Locate platelets.
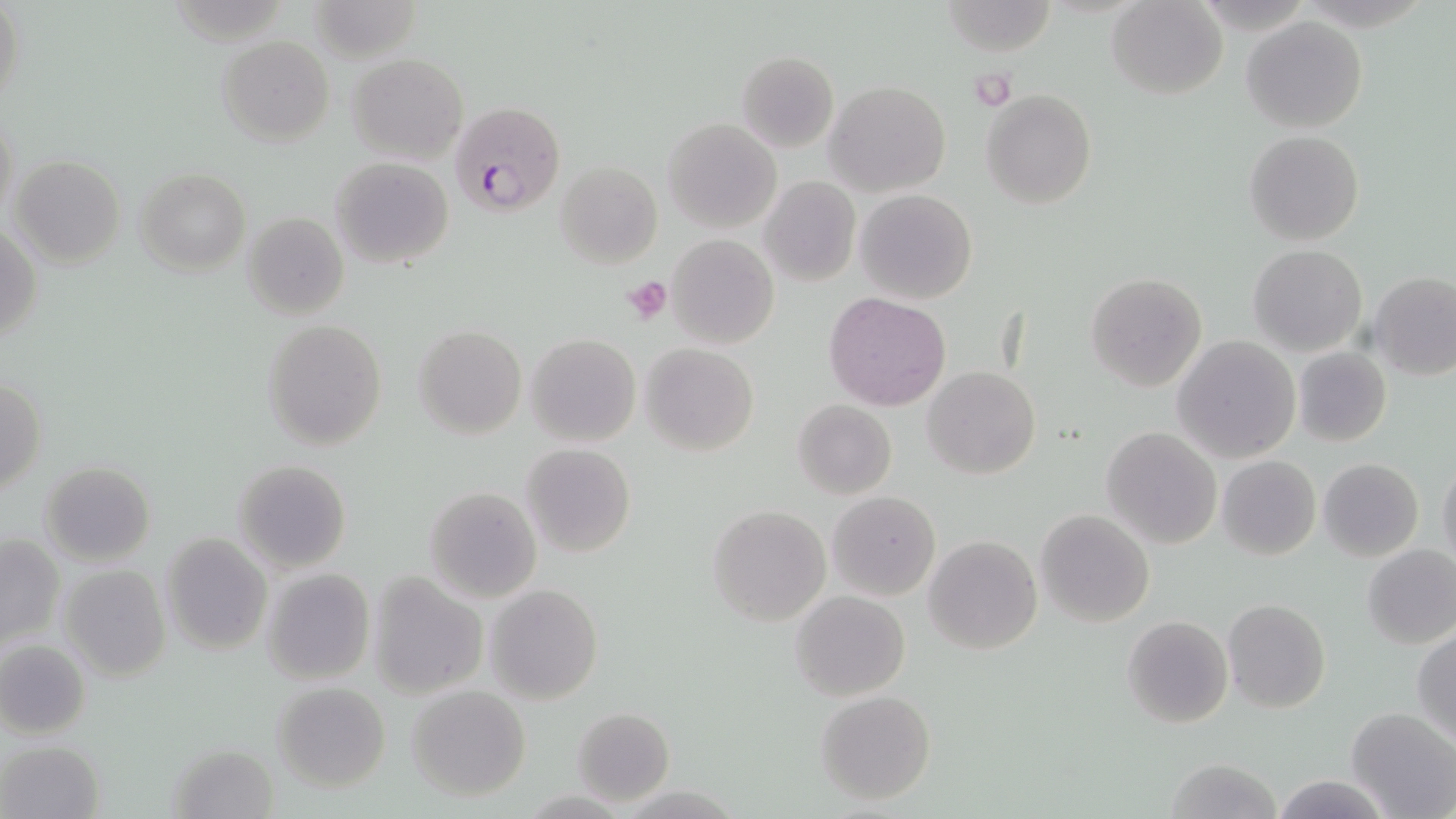

Approximate bounding boxes as (x1, y1, x2, y2) in pixels.
Platelets: (967, 69, 1017, 110), (620, 275, 673, 324).

Plasmodium falciparum-infected red blood cell locations: (452, 102, 564, 217). Uninfected red blood cell locations: (0, 0, 26, 117), (940, 0, 1055, 56), (1107, 1, 1227, 99), (1241, 15, 1369, 133), (217, 35, 334, 146), (736, 51, 838, 152), (348, 52, 468, 164), (824, 81, 951, 198), (981, 90, 1097, 210), (1, 111, 19, 229), (662, 118, 781, 234), (1245, 129, 1364, 246), (8, 155, 126, 269), (329, 157, 454, 270), (555, 161, 662, 268), (135, 168, 250, 275), (760, 176, 860, 286), (855, 189, 977, 306), (242, 212, 350, 319), (2, 224, 42, 347), (667, 234, 779, 350), (1249, 245, 1370, 356), (1369, 270, 1456, 380), (1085, 273, 1208, 393), (824, 292, 950, 411), (264, 318, 386, 450), (413, 325, 526, 439), (525, 333, 641, 447), (1173, 336, 1300, 463), (641, 342, 759, 455), (1293, 346, 1391, 446), (923, 367, 1040, 480), (1, 378, 46, 493), (792, 401, 897, 499), (1101, 427, 1221, 549), (521, 443, 635, 558), (1217, 455, 1320, 560), (1318, 457, 1423, 561), (1438, 458, 1456, 570), (234, 459, 351, 573), (41, 462, 155, 567), (424, 486, 541, 602), (828, 490, 940, 599), (708, 505, 830, 627), (1035, 509, 1155, 627), (0, 533, 65, 650), (160, 534, 272, 654), (923, 535, 1043, 655), (1363, 544, 1456, 650), (59, 564, 171, 681), (262, 567, 375, 684), (368, 573, 486, 700), (485, 583, 603, 704), (789, 590, 910, 701), (1224, 599, 1332, 715), (1122, 616, 1232, 728), (1412, 628, 1456, 744), (0, 640, 90, 738), (272, 682, 390, 792), (406, 685, 531, 801), (816, 691, 936, 806), (572, 707, 675, 805), (1346, 708, 1456, 819), (2, 740, 104, 818), (168, 742, 281, 817), (1164, 759, 1284, 818), (1269, 773, 1394, 818). Slide-level diagnosis: Plasmodium falciparum. Light microscopy. May-Grünwald-Giemsa stain. Image is 1456×819 pixels. Captured at 1000x magnification. One field of a larger specimen. Thin blood film.